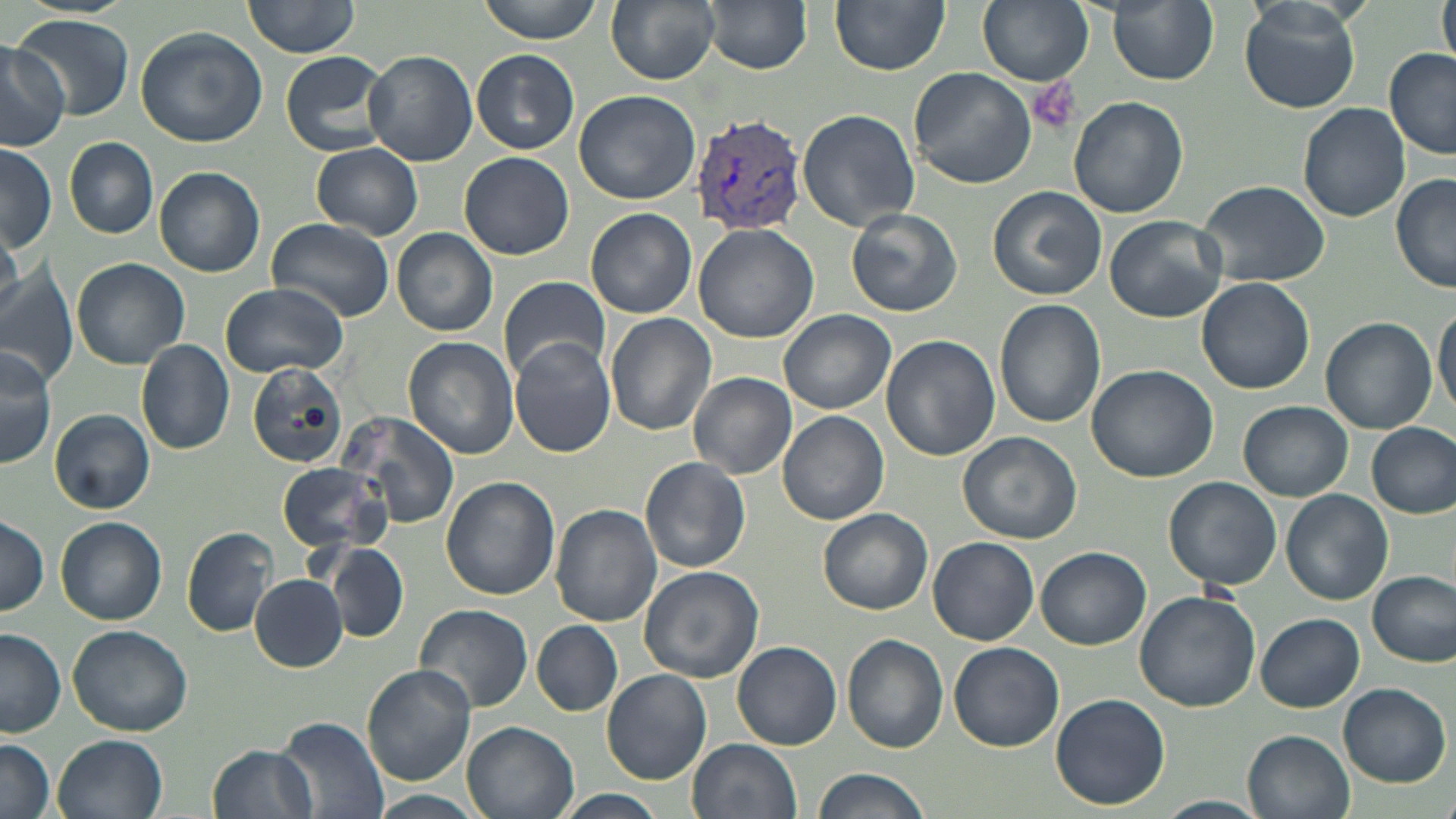

slide-level diagnosis = Plasmodium vivax
uninfected red blood cell locations = approximate bounding boxes as (x1, y1, x2, y2) in pixels: (242, 0, 364, 59), (477, 0, 603, 42), (605, 0, 720, 85), (704, 0, 813, 74), (831, 0, 951, 74), (979, 0, 1093, 86), (1108, 0, 1219, 85), (1437, 0, 1456, 70), (1239, 2, 1361, 113), (13, 15, 136, 121), (134, 27, 267, 148), (0, 42, 69, 150), (363, 49, 479, 167), (278, 50, 392, 157), (472, 50, 580, 155), (1384, 50, 1456, 161), (909, 67, 1036, 188), (573, 89, 701, 205), (1068, 95, 1188, 219), (1297, 103, 1410, 222), (797, 108, 920, 231), (65, 137, 159, 238), (312, 142, 423, 239), (0, 146, 57, 252), (459, 151, 575, 260), (154, 167, 265, 277), (1390, 174, 1456, 294), (1198, 178, 1331, 287), (987, 185, 1106, 301), (846, 207, 961, 318), (586, 208, 696, 318), (1104, 214, 1229, 324), (266, 219, 397, 324), (693, 223, 821, 344), (0, 227, 27, 327), (392, 228, 498, 337), (73, 257, 191, 368), (0, 265, 76, 384), (497, 275, 609, 385), (1197, 277, 1315, 395), (219, 281, 349, 378), (993, 298, 1106, 429), (1434, 303, 1456, 418), (776, 309, 896, 415), (606, 313, 717, 437), (1320, 317, 1436, 433), (880, 334, 1000, 462), (509, 335, 617, 458), (403, 337, 517, 460), (136, 340, 236, 454), (1, 345, 58, 468), (246, 362, 351, 471), (1086, 363, 1219, 482), (688, 371, 797, 479), (1239, 401, 1353, 501), (49, 409, 154, 513), (339, 410, 462, 531), (777, 411, 889, 526), (1369, 422, 1455, 517), (957, 432, 1082, 545), (639, 457, 750, 574), (276, 461, 392, 555), (1164, 475, 1282, 590), (441, 477, 559, 602), (1281, 489, 1391, 604), (552, 505, 661, 624), (817, 507, 932, 615), (0, 514, 50, 616), (56, 516, 167, 624), (183, 526, 278, 636), (928, 536, 1040, 645), (322, 543, 410, 641), (1036, 545, 1150, 650), (637, 566, 764, 683), (1370, 570, 1454, 667), (250, 574, 348, 672), (1133, 590, 1262, 713), (414, 603, 533, 713), (1255, 613, 1364, 711), (533, 621, 622, 717), (68, 624, 193, 735), (0, 629, 67, 737), (842, 635, 949, 753), (732, 640, 843, 750), (948, 641, 1065, 752), (361, 664, 477, 787), (602, 668, 712, 785), (1336, 683, 1451, 789), (1050, 692, 1170, 810), (275, 716, 388, 819), (461, 719, 579, 819), (1244, 729, 1354, 819), (54, 734, 168, 819), (0, 737, 56, 819), (687, 738, 802, 819), (207, 742, 319, 819), (809, 766, 933, 819), (371, 791, 486, 819), (554, 791, 668, 819), (1156, 795, 1270, 819)
modality = light microscopy
field of view = single
stain = May-Grünwald-Giemsa
Plasmodium vivax-infected red blood cell locations = approximate bounding boxes as (x1, y1, x2, y2) in pixels: (692, 113, 807, 235)
image size = 1456×819 pixels
platelet locations = approximate bounding boxes as (x1, y1, x2, y2) in pixels: (1025, 76, 1081, 135)
preparation = thin blood film
magnification = 1000x